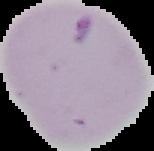

image size = 154×151 pixels
malaria status = parasitized
image type = segmented cell region with the area outside set to black
preparation = thin blood film